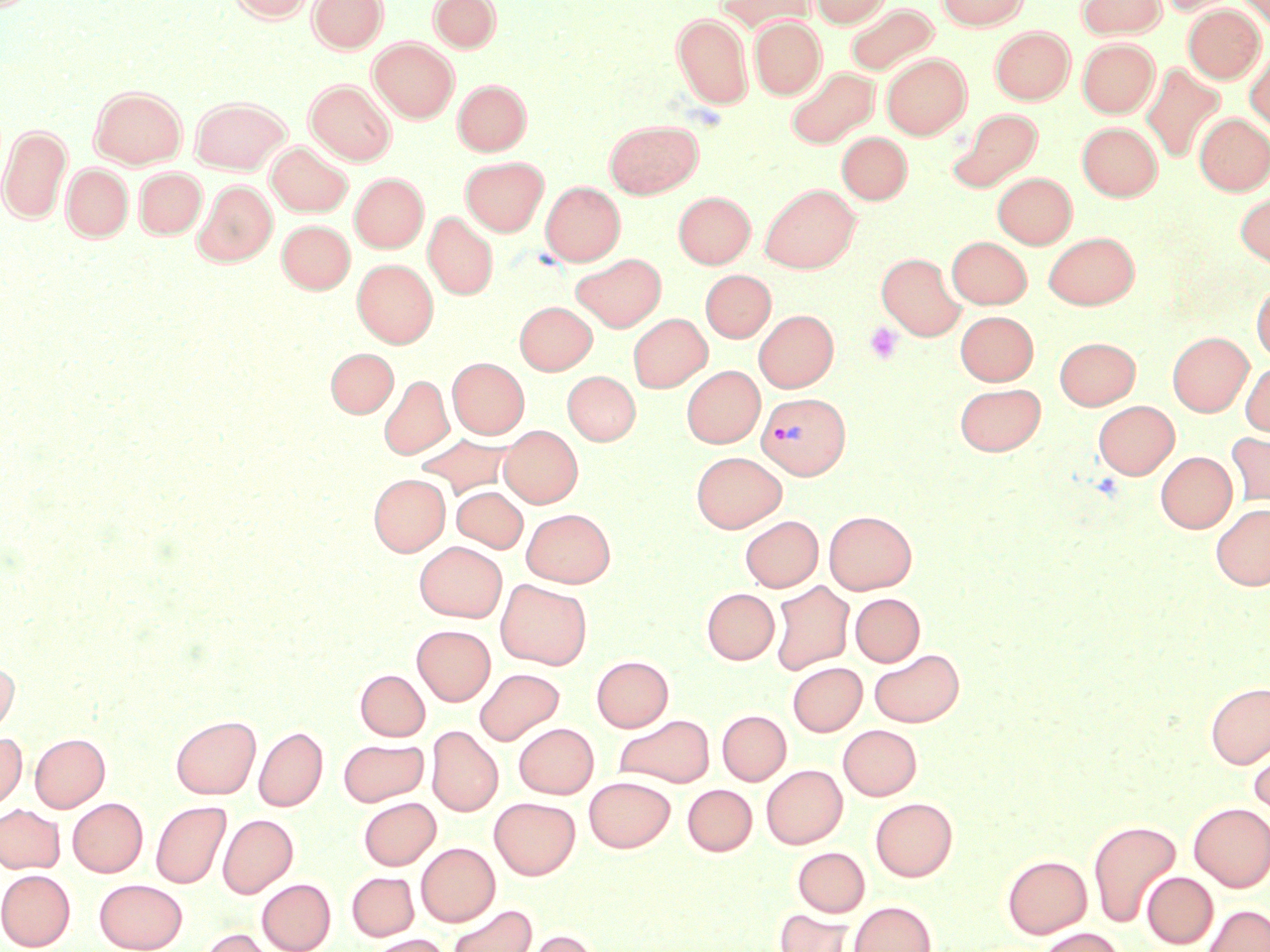
slide_level_diagnosis: Plasmodium vivax
stain: May-Grünwald-Giemsa
platelet_locations: 'approximate bounding boxes as (x1,y1)-(x2,y2) corner pairs in pixels: (864,322)-(904,364)'
field_of_view: single
uninfected_red_blood_cell_locations: 'approximate bounding boxes as (x1,y1)-(x2,y2) corner pairs in pixels: (229,0)-(315,22), (308,0)-(388,53), (717,0)-(815,33), (810,0)-(891,27), (937,0)-(1029,29), (1075,0)-(1166,39), (1157,0)-(1241,16), (1237,0)-(1270,30), (429,1)-(501,53), (846,3)-(938,75), (1183,4)-(1265,83), (673,14)-(752,108), (749,17)-(826,99), (990,26)-(1074,104), (369,38)-(458,122), (1078,39)-(1158,117), (1245,49)-(1270,131), (882,54)-(971,139), (1140,63)-(1225,163), (786,67)-(879,149), (453,79)-(531,155), (306,80)-(395,165), (90,86)-(186,168), (190,96)-(290,174), (948,108)-(1043,192), (1195,113)-(1270,194), (605,121)-(703,197), (1077,122)-(1162,200), (0,124)-(72,223), (837,132)-(911,204), (267,143)-(352,216), (461,156)-(548,235), (62,163)-(132,241), (134,168)-(206,239), (993,172)-(1076,248), (350,173)-(428,252), (194,181)-(277,266), (541,181)-(625,265), (760,184)-(860,272), (674,191)-(755,268), (1235,192)-(1270,269), (424,212)-(497,299), (276,220)-(355,293), (1044,232)-(1139,308), (946,236)-(1031,308), (572,253)-(666,331), (876,253)-(964,340), (353,259)-(438,347), (701,270)-(775,342), (1251,281)-(1270,362), (515,301)-(596,374), (754,310)-(839,391), (955,310)-(1038,385), (628,313)-(712,392), (1168,332)-(1253,416), (1055,336)-(1140,408), (326,348)-(398,417), (447,357)-(529,438), (1240,360)-(1270,437), (681,365)-(764,447), (562,371)-(640,444), (379,375)-(453,460), (954,382)-(1045,456), (1093,400)-(1179,479), (500,425)-(582,507), (1226,431)-(1270,509), (417,434)-(517,499), (691,451)-(786,532), (1155,451)-(1237,532), (369,473)-(449,556), (452,486)-(528,552), (1211,503)-(1270,590), (521,508)-(615,587), (824,510)-(916,594), (740,515)-(823,592), (415,541)-(507,622), (496,579)-(592,669), (769,580)-(854,675), (702,587)-(779,664), (851,593)-(925,666), (412,624)-(496,705), (869,648)-(965,727), (591,656)-(673,731), (0,657)-(19,737), (788,662)-(867,736), (474,667)-(564,745), (355,669)-(430,741), (1205,682)-(1270,768), (717,710)-(791,785), (171,714)-(260,799), (614,714)-(715,788), (514,722)-(598,798), (838,724)-(922,800), (254,726)-(327,811), (427,726)-(503,816), (0,732)-(26,812), (30,733)-(109,812), (338,738)-(428,806), (1249,740)-(1270,820), (761,764)-(847,848), (584,776)-(674,852), (682,784)-(757,855), (359,797)-(440,869), (489,797)-(580,879), (870,797)-(957,881), (67,798)-(147,877), (151,800)-(231,889), (1188,802)-(1270,891), (0,804)-(64,873), (218,814)-(298,898), (1088,819)-(1181,928), (416,842)-(500,926), (793,847)-(870,916), (1002,855)-(1092,938), (0,869)-(76,950), (346,872)-(419,941), (1142,872)-(1218,948), (257,878)-(335,952), (94,879)-(187,952), (848,901)-(936,952), (446,904)-(537,952), (1202,904)-(1270,952), (774,908)-(862,952), (198,927)-(281,952), (1036,927)-(1125,952), (521,929)-(603,952), (367,934)-(453,952)'
image_size: 1270×952 pixels
preparation: thin blood smear
modality: optical microscopy
plasmodium_vivax_infected_red_blood_cell_locations: 'approximate bounding boxes as (x1,y1)-(x2,y2) corner pairs in pixels: (757,392)-(850,479)'
magnification: 1000x